Assess this cell for malaria.
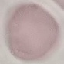
Uninfected.

{
  "preparation": "thin blood film",
  "stain": "Giemsa",
  "capture": "smartphone through the microscope eyepiece",
  "image_type": "cell patch, automatically extracted from a larger field of view and resized to 64 × 64 pixels"
}